Report the malaria status of this cell.
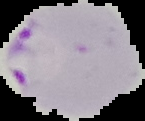

Parasitized.

image size = 145×121 pixels
image type = segmented cell region with the area outside set to black
preparation = thin blood smear